Locate every Plasmodium falciparum-infected red blood cell.
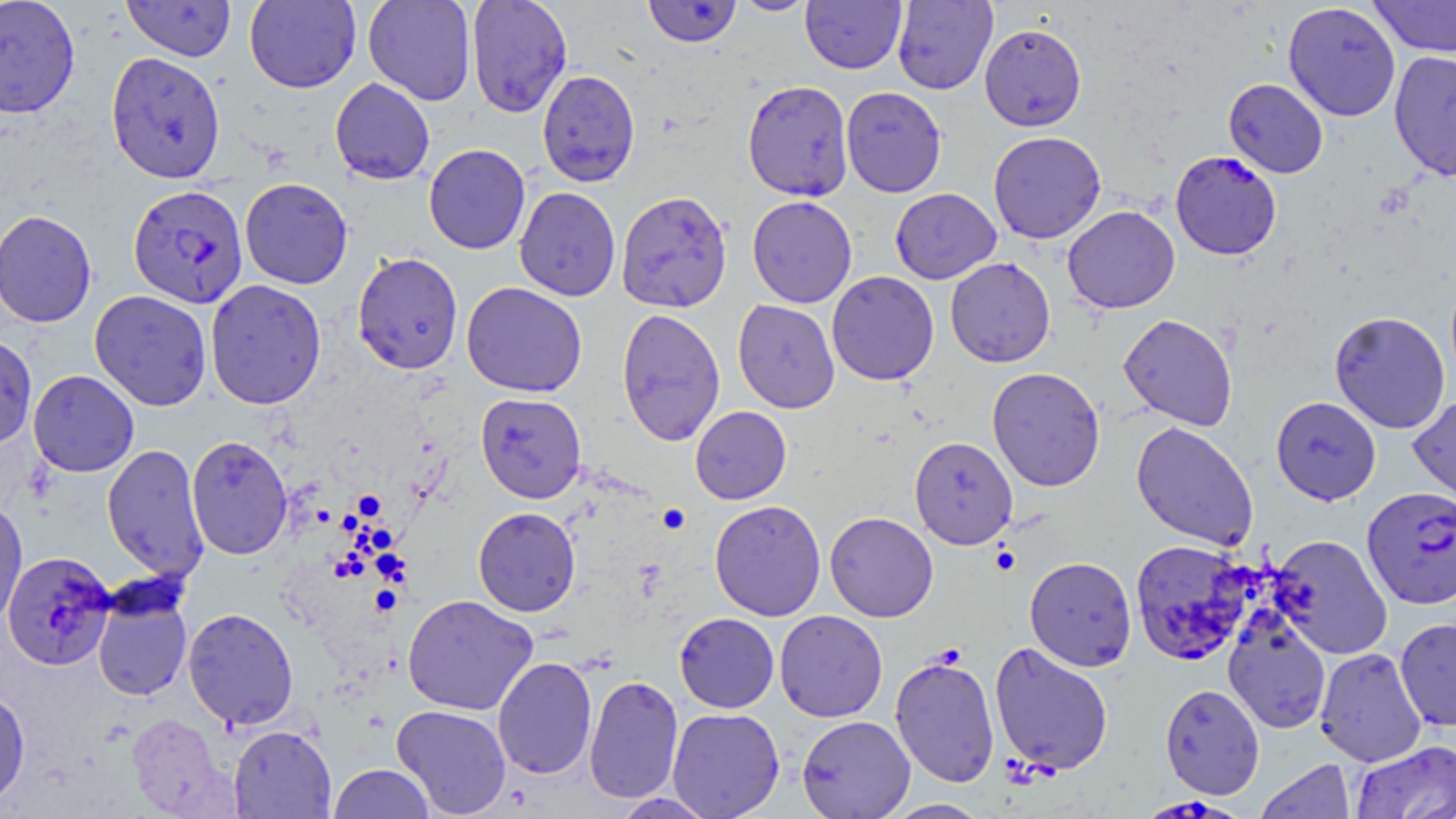

Approximate bounding boxes as (x1,y1)-(x2,y2) corner pairs in pixels.
Plasmodium falciparum-infected red blood cells: (1170,151)-(1282,260), (127,184)-(249,308), (1362,486)-(1456,609), (3,551)-(116,670), (1152,795)-(1244,819).

{
  "slide_level_diagnosis": "Plasmodium falciparum",
  "uninfected_red_blood_cell_locations": "approximate bounding boxes as (x1,y1)-(x2,y2) corner pairs in pixels: (0,0)-(81,118), (244,0)-(361,93), (363,0)-(477,105), (466,0)-(573,117), (642,0)-(743,48), (730,0)-(818,16), (1368,0)-(1456,57), (121,1)-(236,62), (801,1)-(907,74), (892,1)-(998,94), (1282,2)-(1401,122), (979,23)-(1087,131), (1388,50)-(1456,181), (106,52)-(226,183), (537,69)-(640,186), (330,78)-(435,184), (1223,79)-(1328,178), (742,80)-(853,201), (841,86)-(947,197), (988,131)-(1106,244), (423,144)-(531,254), (240,177)-(353,289), (514,187)-(621,301), (890,188)-(1001,284), (616,191)-(732,313), (747,195)-(857,308), (1062,206)-(1180,314), (0,209)-(98,328), (351,251)-(463,374), (945,257)-(1055,368), (826,271)-(939,385), (205,279)-(326,410), (461,282)-(587,398), (89,289)-(212,411), (732,299)-(840,414), (616,308)-(726,446), (1328,311)-(1451,433), (1118,313)-(1238,431), (0,333)-(38,450), (987,367)-(1106,492), (28,370)-(139,477), (475,392)-(587,503), (1408,394)-(1456,510), (1270,396)-(1381,505), (690,406)-(792,504), (1131,421)-(1258,551), (186,434)-(293,560), (909,436)-(1018,549), (102,444)-(209,583), (0,495)-(28,628), (709,500)-(826,621), (473,507)-(581,617), (824,511)-(939,622), (1268,535)-(1393,658), (1129,539)-(1254,665), (1024,556)-(1136,671), (92,586)-(193,702), (402,594)-(539,715), (183,607)-(299,730), (774,610)-(888,722), (675,612)-(779,713), (1223,612)-(1331,734), (1394,617)-(1456,731), (989,641)-(1114,777), (1314,647)-(1428,767), (889,654)-(1000,789), (493,657)-(598,779), (584,674)-(684,803), (1159,683)-(1265,798), (0,687)-(30,808), (391,704)-(512,817), (667,707)-(785,819), (127,712)-(235,818), (797,715)-(915,819), (228,725)-(337,818), (1351,740)-(1456,819), (1256,760)-(1355,819), (329,764)-(435,818), (610,792)-(719,819), (882,798)-(992,818)",
  "magnification": "1000x",
  "image_size": "1456×819 pixels",
  "modality": "optical microscopy",
  "stain": "May-Grünwald-Giemsa",
  "field_of_view": "single",
  "preparation": "thin blood smear"
}